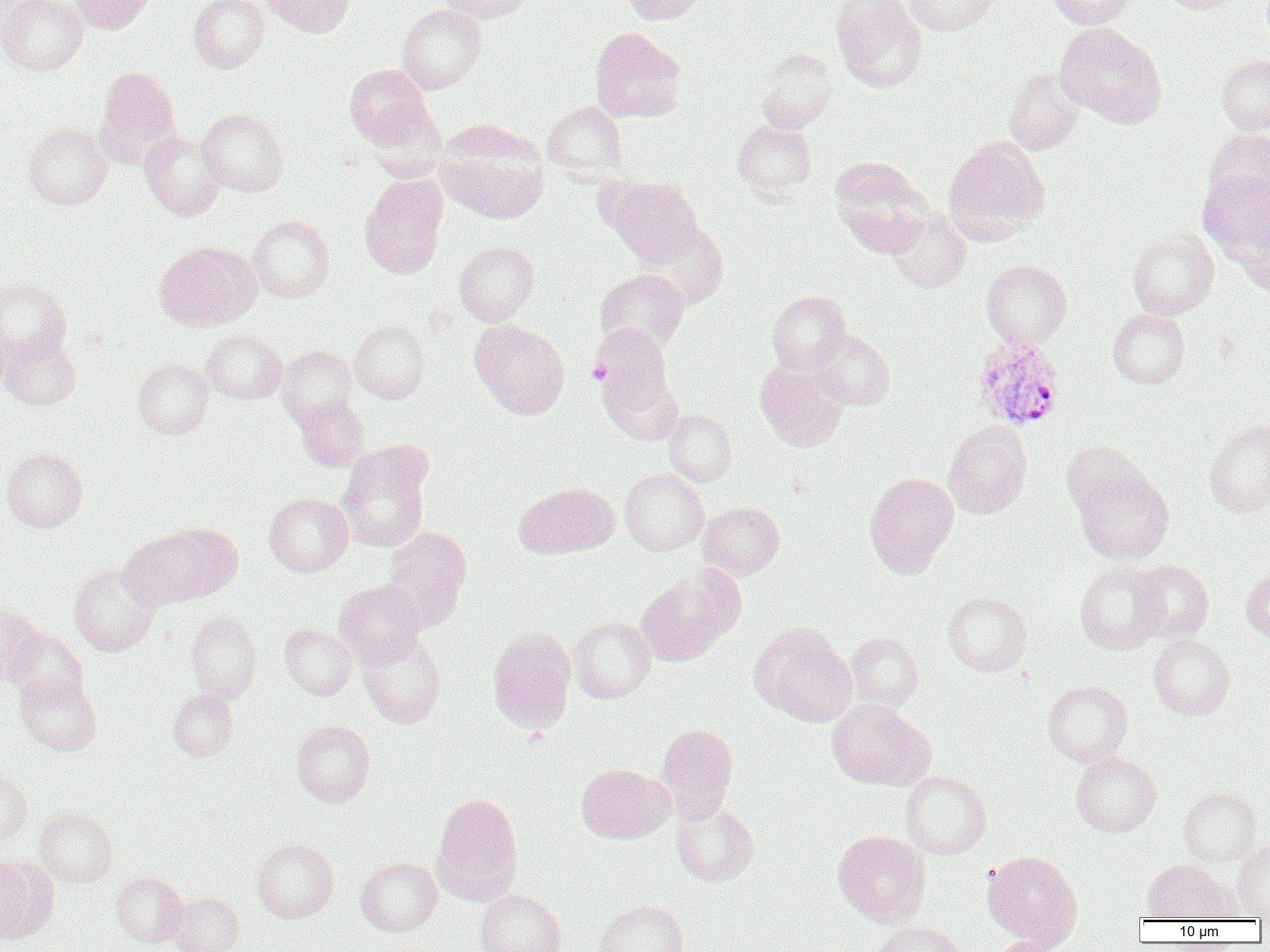 Approximate bounding boxes as (x1,y1)-(x2,y2) corner pairs in pixels. Uninfected red blood cell locations: (0,0)-(86,74), (71,0)-(153,33), (189,0)-(268,73), (262,0)-(355,36), (438,0)-(534,22), (621,0)-(708,24), (831,0)-(927,92), (905,0)-(999,36), (1049,0)-(1134,29), (1157,0)-(1244,13), (398,4)-(486,93), (1055,22)-(1166,128), (589,27)-(687,123), (756,51)-(836,134), (1217,54)-(1270,135), (345,63)-(434,147), (96,66)-(180,159), (1003,68)-(1084,155), (543,101)-(627,179), (197,108)-(289,196), (435,119)-(549,223), (732,120)-(816,198), (25,124)-(111,209), (1204,128)-(1270,214), (140,131)-(225,220), (943,137)-(1050,241), (829,156)-(933,256), (1197,169)-(1270,263), (360,174)-(448,278), (607,178)-(702,265), (886,208)-(970,292), (1240,214)-(1270,297), (248,215)-(334,302), (635,223)-(729,309), (1127,229)-(1219,320), (154,241)-(260,330), (454,241)-(539,326), (981,259)-(1072,348), (595,268)-(689,354), (0,279)-(72,365), (767,291)-(851,373), (1107,309)-(1190,389), (470,319)-(570,418), (350,320)-(430,403), (591,324)-(677,425), (808,329)-(894,409), (202,330)-(287,403), (0,333)-(81,409), (277,345)-(356,427), (134,359)-(212,438), (756,361)-(848,451), (296,394)-(369,471), (664,409)-(736,485), (1204,420)-(1270,516), (943,422)-(1032,518), (1061,440)-(1147,516), (2,449)-(88,531), (337,450)-(430,552), (1072,465)-(1174,563), (620,469)-(708,554), (864,471)-(959,577), (514,482)-(618,558), (264,493)-(353,575), (697,502)-(784,578), (165,524)-(243,598), (381,528)-(472,631), (120,529)-(211,609), (1131,560)-(1214,642), (1074,562)-(1168,654), (69,563)-(161,656), (635,567)-(742,666), (1241,569)-(1270,644), (334,580)-(425,667), (943,591)-(1032,676), (0,605)-(45,685), (185,610)-(262,703), (570,617)-(655,703), (280,623)-(356,699), (751,623)-(858,725), (487,628)-(576,732), (7,629)-(88,704), (359,632)-(445,728), (846,632)-(923,710), (1148,635)-(1234,719), (14,672)-(102,755), (1043,680)-(1133,766), (168,689)-(238,760), (827,699)-(932,790), (292,719)-(375,806), (656,723)-(738,820), (1071,752)-(1161,836), (576,763)-(674,843), (0,770)-(32,846), (901,771)-(991,859), (1179,787)-(1261,866), (430,791)-(524,907), (671,803)-(758,885), (35,807)-(118,886), (833,830)-(931,926), (251,838)-(339,922), (1232,839)-(1270,919), (983,850)-(1083,950), (0,857)-(45,940), (356,857)-(441,936), (1143,860)-(1229,922), (111,871)-(187,946), (476,890)-(566,952), (168,891)-(244,952), (594,900)-(689,952), (875,921)-(964,952), (988,937)-(1064,952). Plasmodium ovale-infected red blood cell locations: (971,335)-(1065,431). Platelet locations: (588,360)-(610,385). Slide-level diagnosis: Plasmodium ovale. Optical microscopy. Thin blood smear. Single field of view. Image is 1270×952 pixels. 1000x magnification.